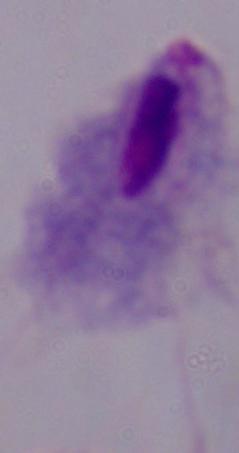

Summary:
  - Modality: micrograph
  - Identification: trichomonad
  - Magnification: 1000x